Name the cell type shown.
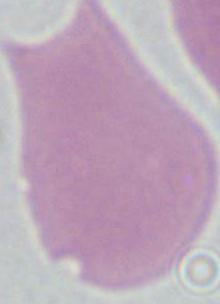
This is an erythrocyte.

1000x magnification. Micrograph.